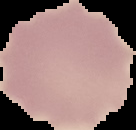
{
  "image_size": "136×130 pixels",
  "image_type": "cell region segmented out of the field of view; surrounding area masked to black",
  "preparation": "thin blood smear",
  "malaria_status": "uninfected"
}